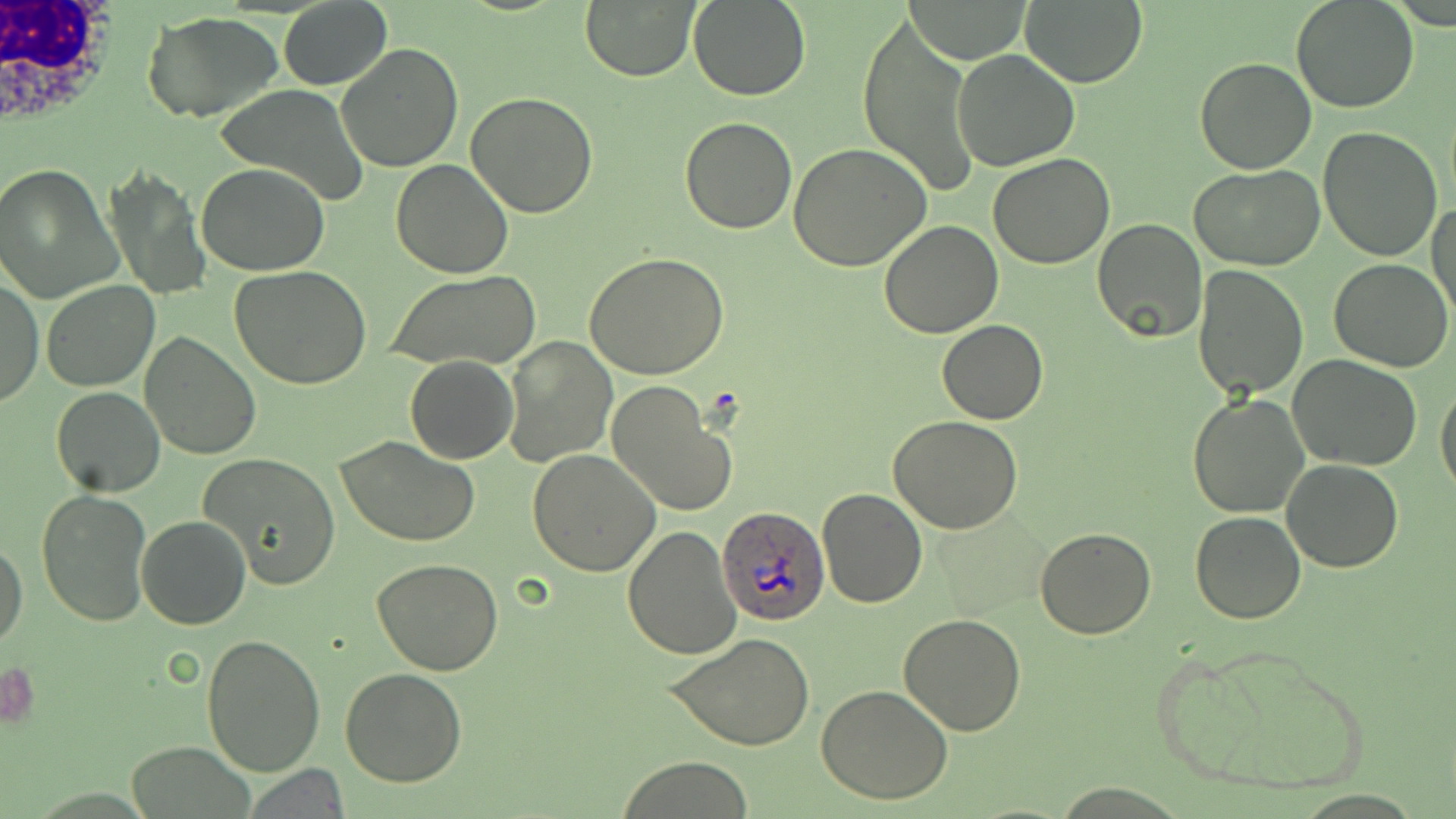
Plasmodium ovale-infected red blood cell locations = approximate bounding boxes as (x1, y1, x2, y2) in pixels: (718, 506, 828, 625)
slide-level diagnosis = Plasmodium ovale
modality = optical microscopy
stain = May-Grünwald-Giemsa
uninfected red blood cell locations = approximate bounding boxes as (x1, y1, x2, y2) in pixels: (580, 0, 703, 82), (912, 0, 1030, 62), (1018, 0, 1147, 86), (1291, 0, 1420, 115), (277, 1, 393, 91), (688, 1, 813, 101), (142, 11, 284, 123), (857, 12, 979, 198), (334, 43, 463, 173), (950, 50, 1080, 172), (1193, 57, 1319, 174), (217, 82, 367, 203), (465, 90, 598, 217), (680, 117, 797, 234), (1317, 126, 1443, 263), (788, 143, 932, 270), (987, 154, 1115, 270), (392, 158, 512, 278), (197, 162, 328, 276), (0, 163, 121, 303), (1192, 163, 1325, 271), (102, 164, 212, 301), (1430, 198, 1456, 323), (1092, 217, 1209, 344), (879, 219, 1004, 337), (584, 251, 730, 379), (1329, 257, 1454, 371), (1193, 264, 1307, 399), (230, 265, 373, 389), (387, 269, 543, 371), (1, 273, 43, 410), (41, 280, 159, 392), (936, 319, 1049, 424), (139, 330, 263, 460), (502, 336, 615, 467), (404, 356, 520, 464), (1287, 356, 1426, 473), (1435, 376, 1456, 501), (606, 381, 737, 516), (49, 386, 166, 497), (1187, 392, 1308, 518), (889, 418, 1023, 534), (336, 436, 482, 548), (528, 450, 659, 575), (199, 453, 341, 590), (1280, 458, 1404, 572), (817, 486, 927, 607), (36, 489, 152, 626), (1189, 510, 1307, 624), (136, 514, 250, 629), (623, 527, 741, 662), (1035, 528, 1157, 639), (1, 538, 26, 651), (371, 559, 505, 675), (898, 613, 1027, 736), (664, 632, 817, 752), (202, 635, 328, 776), (1152, 640, 1371, 798), (340, 668, 469, 787), (816, 685, 953, 804), (125, 740, 253, 818), (615, 757, 761, 817)
image size = 1456×819 pixels
field of view = single
magnification = 1000x
white blood cell locations = approximate bounding boxes as (x1, y1, x2, y2) in pixels: (0, 0, 127, 139)
preparation = thin blood smear